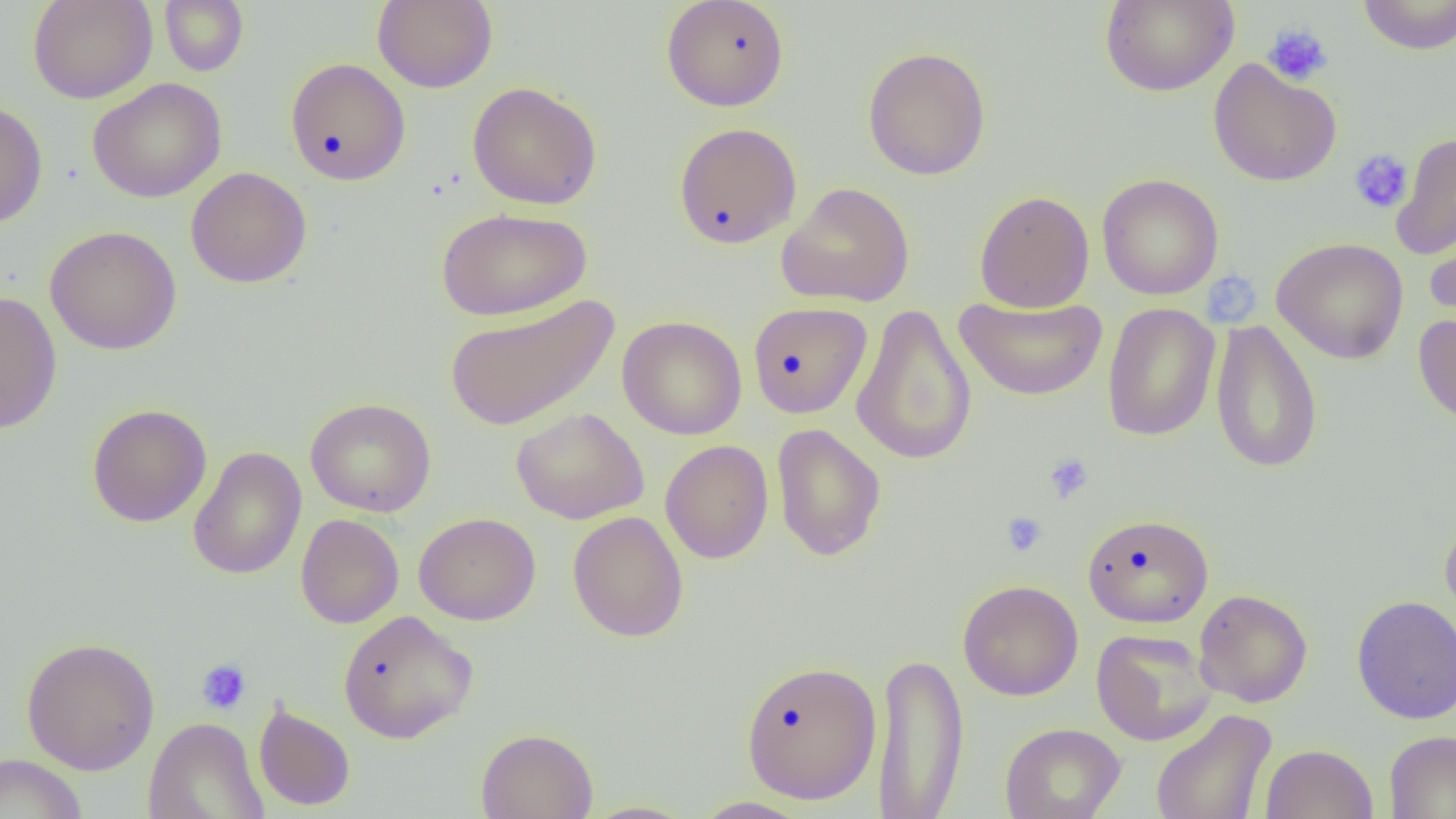
Approximate bounding boxes as (x1,y1)-(x2,y2) corner pairs in pixels. Platelet locations: (1262,23)-(1333,87), (1349,149)-(1413,214), (1212,271)-(1258,321), (1044,452)-(1095,504), (1002,512)-(1048,558), (196,658)-(251,715). Uninfected red blood cell locations: (28,0)-(157,104), (159,0)-(249,76), (1099,0)-(1238,97), (1358,0)-(1456,55), (372,1)-(498,93), (661,1)-(790,111), (862,46)-(992,181), (285,57)-(411,186), (1208,58)-(1342,187), (87,78)-(226,203), (467,82)-(603,210), (0,99)-(48,229), (673,122)-(803,249), (1391,131)-(1456,260), (186,167)-(312,288), (1096,174)-(1224,300), (776,182)-(915,307), (974,190)-(1094,313), (436,208)-(591,322), (1424,221)-(1456,328), (44,226)-(182,355), (1271,237)-(1409,364), (0,290)-(62,435), (444,294)-(618,432), (954,294)-(1107,402), (748,301)-(872,418), (1102,302)-(1220,442), (851,303)-(977,466), (1413,313)-(1456,428), (618,315)-(747,440), (1210,319)-(1323,474), (305,397)-(436,517), (87,404)-(212,527), (511,407)-(649,524), (771,423)-(886,561), (660,440)-(774,564), (188,446)-(306,579), (567,511)-(688,642), (414,512)-(541,626), (1082,513)-(1213,628), (295,514)-(404,628), (1440,515)-(1456,632), (958,579)-(1083,701), (1194,588)-(1313,708), (1351,595)-(1456,724), (337,610)-(477,743), (1091,628)-(1217,745), (20,636)-(160,775), (872,650)-(968,818), (740,659)-(882,805), (253,701)-(356,812), (1150,708)-(1277,819), (143,716)-(268,819), (1000,722)-(1126,818), (475,727)-(598,819), (1384,730)-(1456,818), (1259,743)-(1378,819), (0,753)-(88,819), (689,796)-(815,818), (577,799)-(700,818). Slide-level diagnosis: no evidence of blood parasites. 1000x magnification. Image is 1456×819 pixels. Single field of view. Optical microscopy. Thin blood smear.